Report the malaria status.
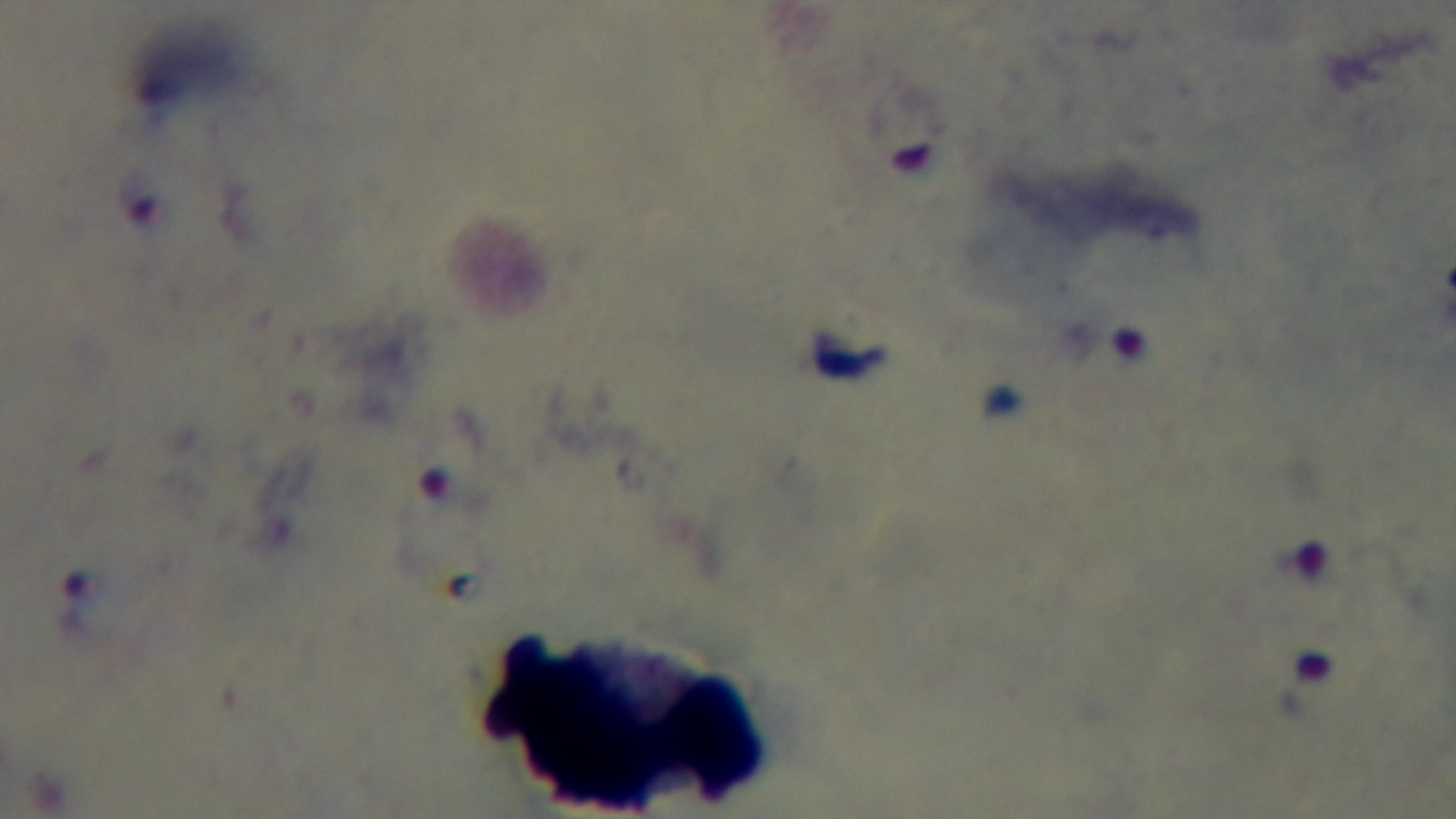

Positive.

Summary:
  - Stain: Giemsa
  - Modality: light microscopy
  - Capture: mounted 4K digital camera
  - Field of view: single
  - Preparation: thick
  - Objective: 100x oil immersion